Assess this cell for malaria.
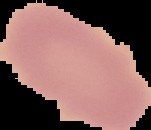
It is uninfected.

image type = segmented cell region on a black background
image size = 151×130 pixels
preparation = thin blood smear